Identify the parasite.
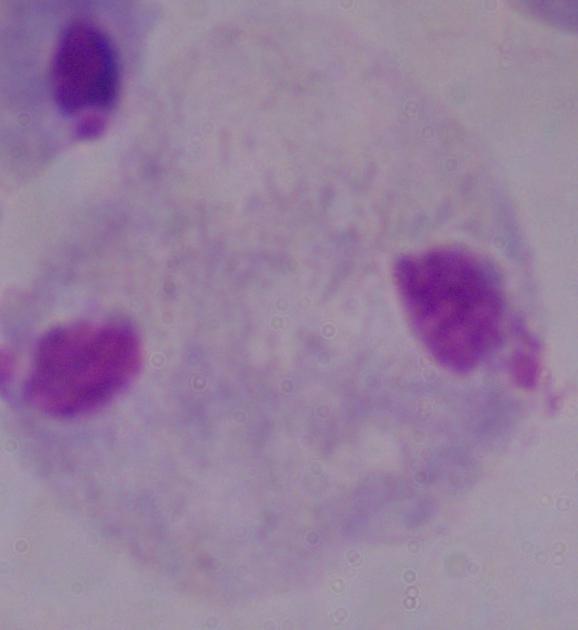
A trichomonad.

Captured at 1000x magnification. Micrograph.